Assess for malaria.
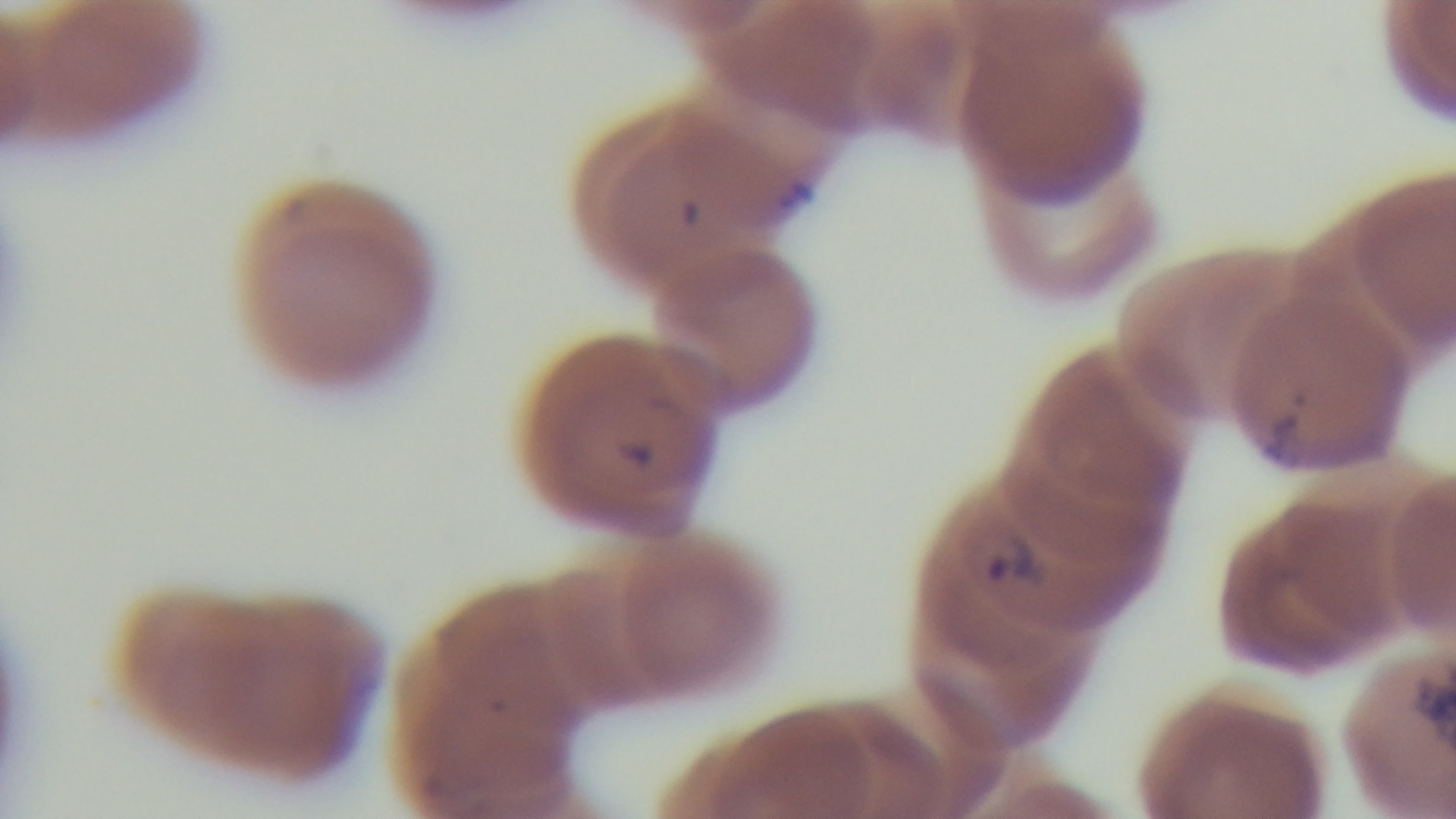

Positive.

Preparation: thin blood film. Mounted 4K digital camera. Giemsa-stained. Single field of view. 100x oil-immersion objective. Light microscopy.